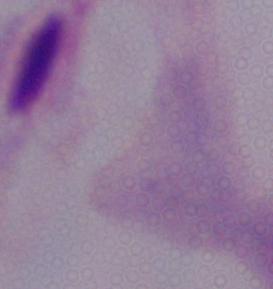
Captured at 1000x magnification. Photomicrograph. A trichomonad is seen.